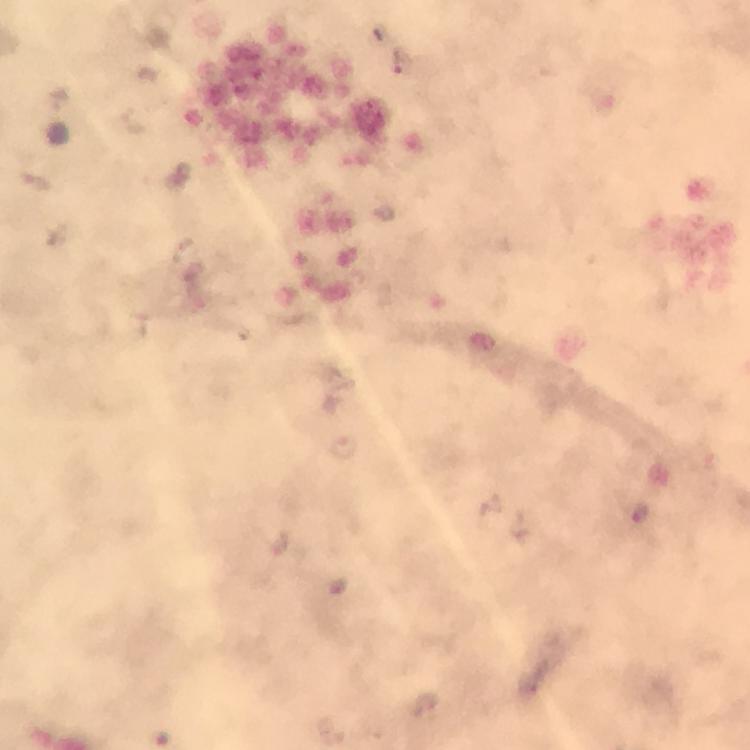

Approximate centers as {x, y} in pixels.
Summary:
  - Plasmodium parasite locations: {401, 61}, {343, 446}, {641, 513}, {425, 704}
  - Magnification: 100x
  - Context: from a malaria diagnostic workup
  - Image size: 750×750 pixels
  - Preparation: thick blood smear
  - Immersion oil: used
  - Capture: smartphone mounted on the microscope
  - Cropped from: one field of view
  - Stain: Giemsa